Comment on the morphology of the erythrocytes.
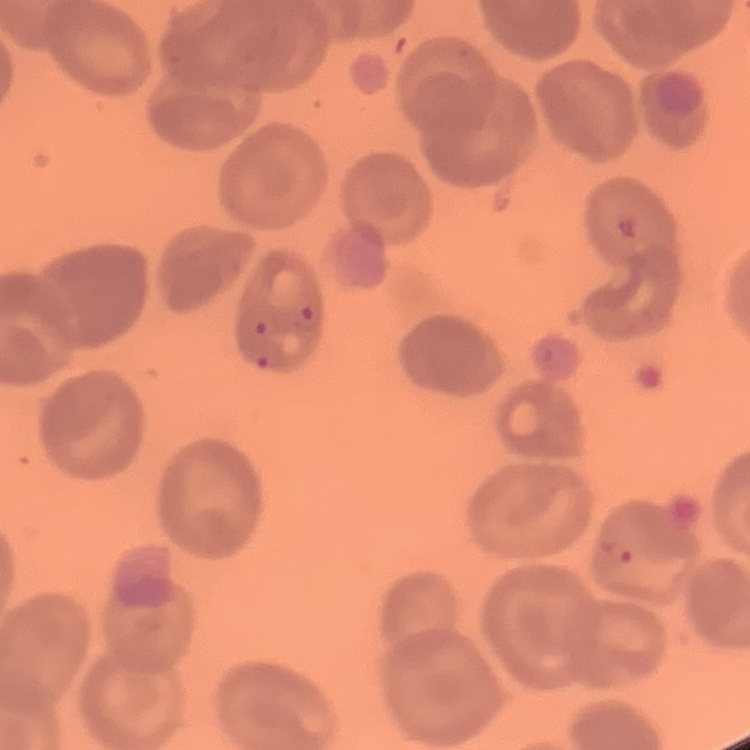

No rouleaux formation.

image_type: square crop of a larger photomicrograph
preparation: thin blood film
stain: Field's or Giemsa